Classify this cell by malaria status.
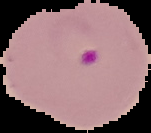

Parasitized.

Summary:
  - Image size: 151×133 pixels
  - Image type: cell region segmented out of the field of view; surrounding area masked to black
  - Preparation: thin blood smear